Locate every blood parasite and identify its species.
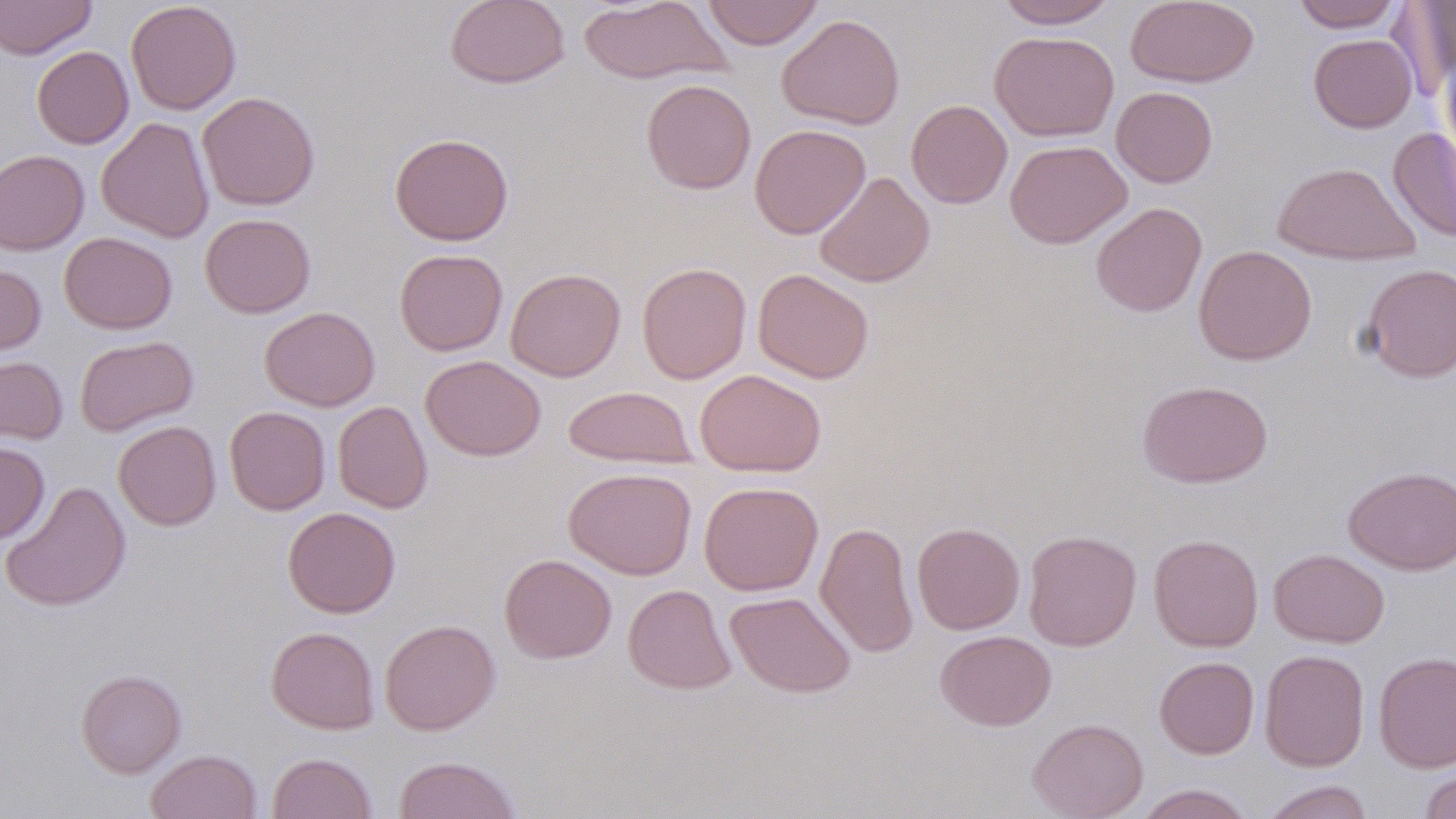
No blood parasites observed.

Approximate bounding boxes as (x1,y1)-(x2,y2) corner pairs in pixels. Uninfected red blood cell locations: (0,0)-(97,59), (125,0)-(241,115), (445,0)-(570,89), (578,0)-(732,85), (702,0)-(823,50), (995,0)-(1119,28), (1125,0)-(1260,88), (1292,0)-(1402,32), (1389,1)-(1456,98), (777,14)-(905,129), (989,31)-(1119,142), (1308,33)-(1417,133), (32,46)-(134,149), (1441,51)-(1456,162), (640,79)-(756,195), (1111,86)-(1219,187), (197,91)-(321,210), (906,99)-(1013,208), (96,116)-(214,243), (749,123)-(870,239), (1388,127)-(1456,243), (389,133)-(514,245), (1005,140)-(1132,249), (0,149)-(89,255), (1271,161)-(1420,265), (814,171)-(935,288), (1090,202)-(1207,317), (200,213)-(316,318), (59,232)-(177,334), (1193,245)-(1317,365), (394,249)-(508,356), (637,262)-(751,384), (0,263)-(46,359), (1360,263)-(1455,383), (505,267)-(625,381), (753,268)-(874,384), (259,306)-(380,411), (75,335)-(198,436), (0,355)-(68,445), (421,355)-(546,461), (695,368)-(827,477), (1137,380)-(1273,487), (563,385)-(697,469), (333,400)-(433,513), (225,406)-(331,515), (113,421)-(221,530), (0,442)-(50,543), (1342,465)-(1456,575), (563,467)-(697,580), (0,481)-(131,611), (699,481)-(823,596), (283,506)-(401,618), (815,520)-(919,658), (912,522)-(1025,635), (1023,529)-(1142,652), (1148,534)-(1263,652), (1269,548)-(1389,648), (500,554)-(617,663), (623,584)-(736,694), (725,591)-(856,698), (379,618)-(501,735), (265,626)-(379,734), (935,630)-(1056,731), (1259,649)-(1370,771), (1373,651)-(1456,773), (1154,656)-(1259,759), (75,669)-(187,778), (1027,717)-(1148,819), (146,749)-(262,819), (267,752)-(378,819), (393,755)-(522,819), (1420,766)-(1456,819), (1259,780)-(1376,819), (1133,783)-(1256,819). Slide-level diagnosis: negative for blood parasites. 1000x magnification. May-Grünwald-Giemsa-stained preparation. Thin blood smear. Light microscopy. Image is 1456×819 pixels. One field of a larger specimen.